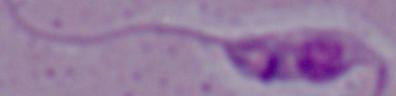 A Leishmania parasite is seen. Captured at 1000x magnification. Micrograph.